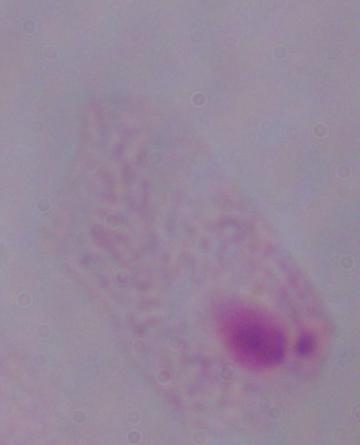 Photomicrograph. A trichomonad is shown. 1000x magnification.